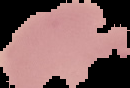
image_size: 130×88 pixels
preparation: thin blood film
malaria_status: uninfected
image_type: segmented cell region on a black background